Locate every Plasmodium vivax-infected red blood cell.
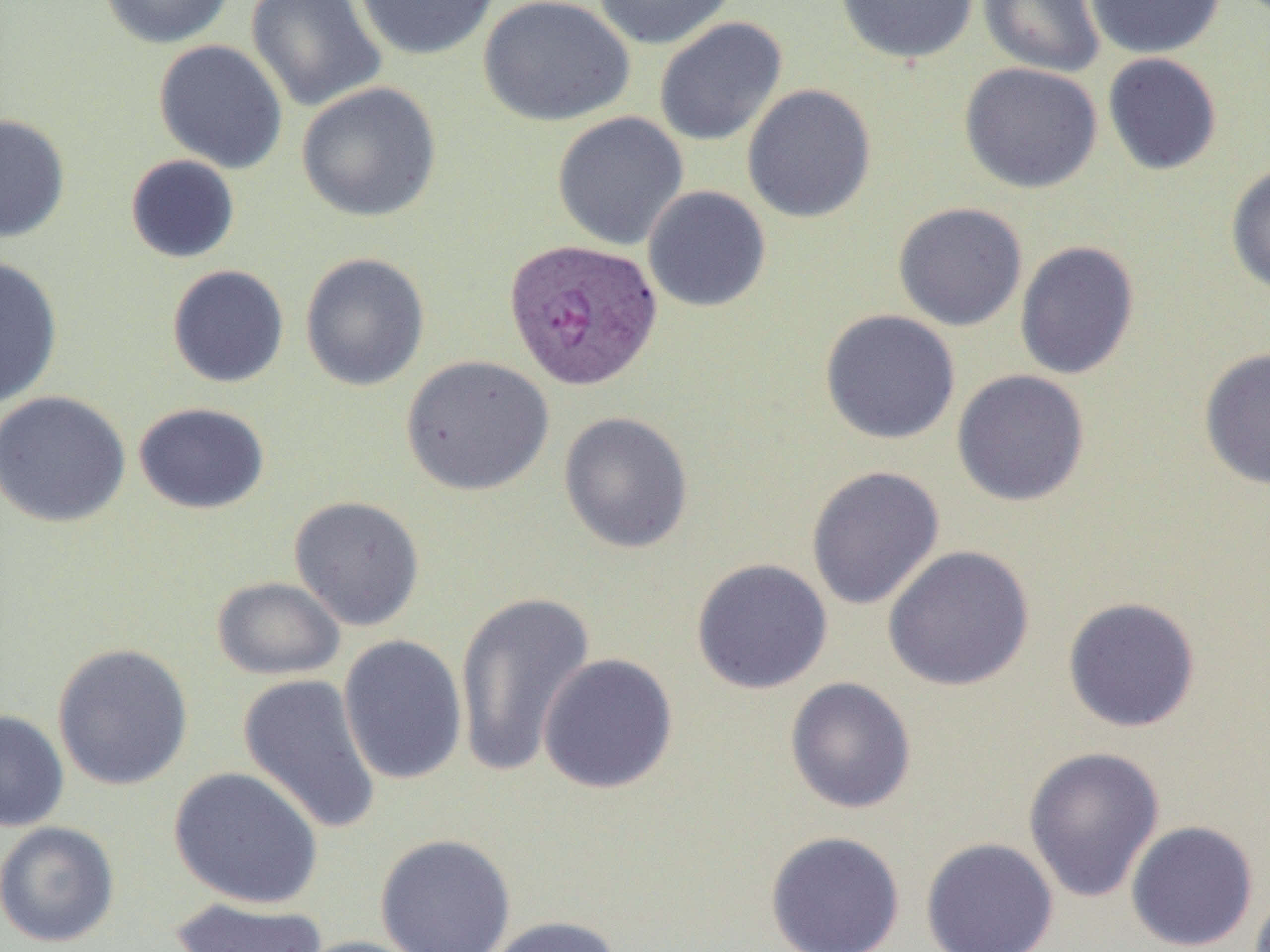
Approximate bounding boxes as (x1, y1, x2, y2) in pixels.
Plasmodium vivax-infected red blood cells: (502, 237, 664, 392).

Uninfected red blood cell locations: (98, 0, 235, 49), (246, 0, 387, 113), (353, 0, 501, 61), (477, 0, 635, 127), (592, 0, 738, 50), (834, 0, 979, 65), (977, 0, 1105, 78), (1084, 0, 1227, 59), (654, 17, 787, 147), (153, 39, 288, 174), (1102, 52, 1222, 175), (959, 62, 1103, 194), (296, 82, 442, 223), (741, 84, 877, 224), (552, 111, 689, 250), (0, 113, 71, 242), (125, 154, 241, 264), (1225, 162, 1270, 297), (642, 186, 771, 312), (892, 202, 1028, 331), (1014, 240, 1140, 380), (299, 252, 430, 392), (0, 256, 64, 410), (166, 264, 289, 388), (819, 309, 961, 445), (1198, 346, 1270, 490), (400, 354, 554, 496), (951, 369, 1090, 507), (0, 390, 133, 528), (133, 402, 270, 514), (558, 411, 694, 554), (805, 464, 945, 610), (288, 495, 425, 631), (882, 545, 1035, 692), (691, 558, 833, 694), (211, 576, 345, 681), (454, 588, 597, 779), (1062, 596, 1201, 732), (337, 635, 468, 786), (52, 643, 194, 791), (537, 653, 679, 795), (237, 672, 383, 837), (785, 677, 917, 814), (0, 709, 69, 832), (1022, 745, 1165, 903), (168, 766, 324, 909), (1125, 820, 1259, 951), (0, 821, 120, 948), (764, 830, 906, 952), (375, 834, 516, 952), (920, 837, 1059, 952), (170, 896, 329, 952), (482, 915, 622, 952), (290, 936, 428, 952). Slide-level diagnosis: Plasmodium vivax. Single field of view. Captured at 1000x magnification. Light microscopy. Image is 1270×952 pixels. Thin blood smear.